Give the extent of all Plasmodium malariae-infected red blood cells.
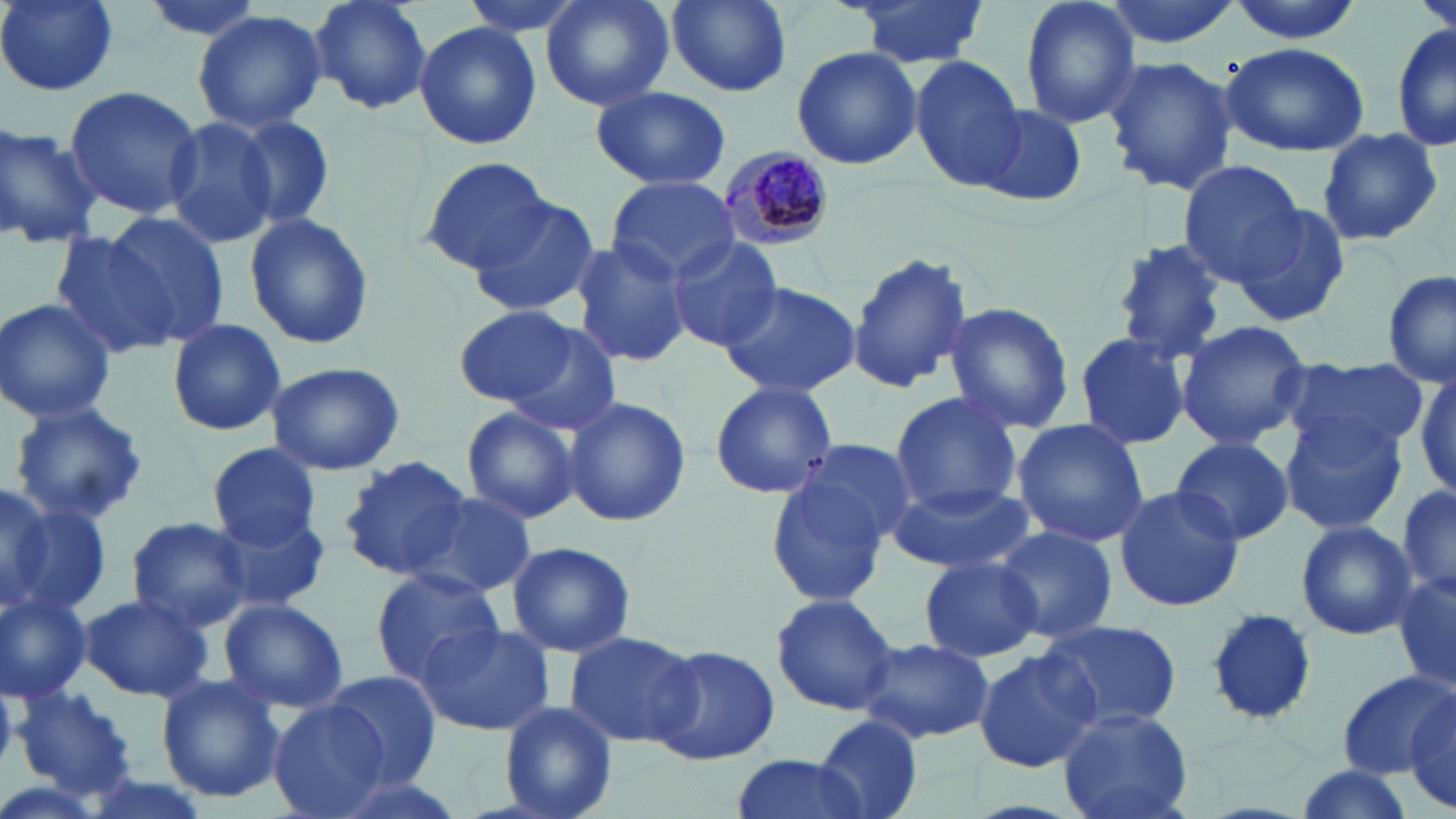
Approximate bounding boxes as [x1, y1, x2, y2] in pixels.
Plasmodium malariae-infected red blood cells: [712, 145, 838, 250].

Summary:
  - Uninfected red blood cell locations: [2, 0, 119, 94], [135, 0, 270, 43], [305, 0, 434, 116], [459, 0, 592, 40], [540, 0, 675, 113], [843, 0, 990, 67], [1019, 0, 1140, 130], [1103, 0, 1242, 49], [1223, 0, 1366, 45], [1413, 0, 1455, 40], [666, 1, 793, 97], [192, 9, 328, 134], [1391, 21, 1455, 155], [413, 22, 542, 151], [1221, 42, 1371, 158], [790, 45, 922, 172], [1101, 54, 1238, 196], [911, 57, 1027, 189], [65, 86, 201, 219], [591, 86, 731, 190], [977, 105, 1089, 207], [233, 112, 337, 231], [164, 115, 282, 251], [0, 120, 100, 249], [1316, 126, 1443, 246], [421, 156, 553, 275], [1177, 159, 1306, 285], [606, 178, 740, 281], [467, 197, 598, 317], [1229, 205, 1351, 328], [99, 212, 229, 346], [246, 212, 375, 351], [53, 229, 178, 362], [569, 236, 694, 370], [663, 238, 783, 354], [1105, 238, 1232, 361], [847, 251, 975, 397], [1382, 270, 1455, 389], [721, 280, 859, 399], [0, 297, 119, 424], [943, 302, 1077, 435], [454, 307, 581, 407], [166, 319, 290, 435], [483, 319, 624, 438], [1174, 320, 1314, 451], [1073, 332, 1195, 452], [1286, 358, 1429, 458], [265, 361, 406, 475], [1409, 368, 1456, 494], [709, 380, 838, 500], [890, 393, 1022, 512], [561, 395, 692, 528], [8, 401, 149, 525], [460, 406, 582, 525], [1279, 415, 1408, 535], [1012, 420, 1149, 545], [1172, 437, 1294, 545], [780, 438, 921, 562], [207, 444, 323, 551], [338, 455, 473, 581], [764, 466, 898, 609], [1396, 480, 1453, 602], [886, 483, 1032, 576], [1114, 484, 1245, 610], [0, 485, 54, 608], [410, 490, 536, 598], [5, 492, 108, 617], [212, 511, 330, 615], [125, 515, 253, 633], [1296, 521, 1418, 641], [990, 524, 1120, 644], [505, 540, 637, 659], [920, 554, 1042, 663], [371, 568, 504, 684], [1393, 573, 1456, 694], [0, 588, 93, 704], [78, 592, 214, 702], [771, 592, 898, 716], [219, 597, 348, 713], [1204, 608, 1316, 726], [1038, 617, 1181, 733], [412, 621, 554, 735], [564, 630, 702, 750], [859, 638, 995, 744], [649, 643, 779, 765], [972, 647, 1101, 774], [324, 670, 442, 787], [1336, 671, 1454, 780], [155, 674, 287, 805], [12, 686, 141, 803], [1406, 692, 1456, 814], [269, 700, 394, 819], [499, 702, 618, 819], [1056, 704, 1194, 819], [815, 715, 923, 819], [728, 753, 878, 819], [1291, 763, 1414, 816], [315, 768, 472, 819]
  - Slide-level diagnosis: Plasmodium malariae
  - Field of view: single
  - Modality: light microscopy
  - Preparation: thin blood film
  - Magnification: 1000x
  - Stain: May-Grünwald-Giemsa
  - Image size: 1456×819 pixels